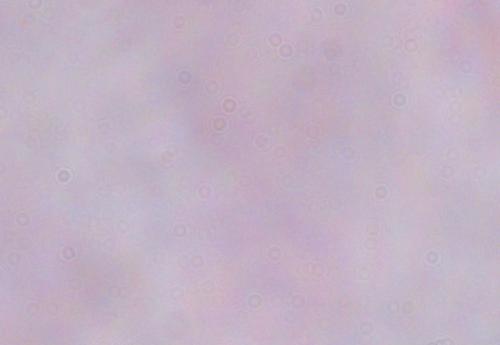
Photomicrograph. 1000x magnification. A trypanosome is shown.